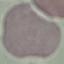
Summary:
  - Result: no malaria parasites detected
  - Image type: cell patch, automatically extracted from a larger field of view and resized to 64 × 64 pixels
  - Preparation: thin smear
  - Capture: smartphone through the microscope eyepiece
  - Stain: Giemsa